State the preparation type.
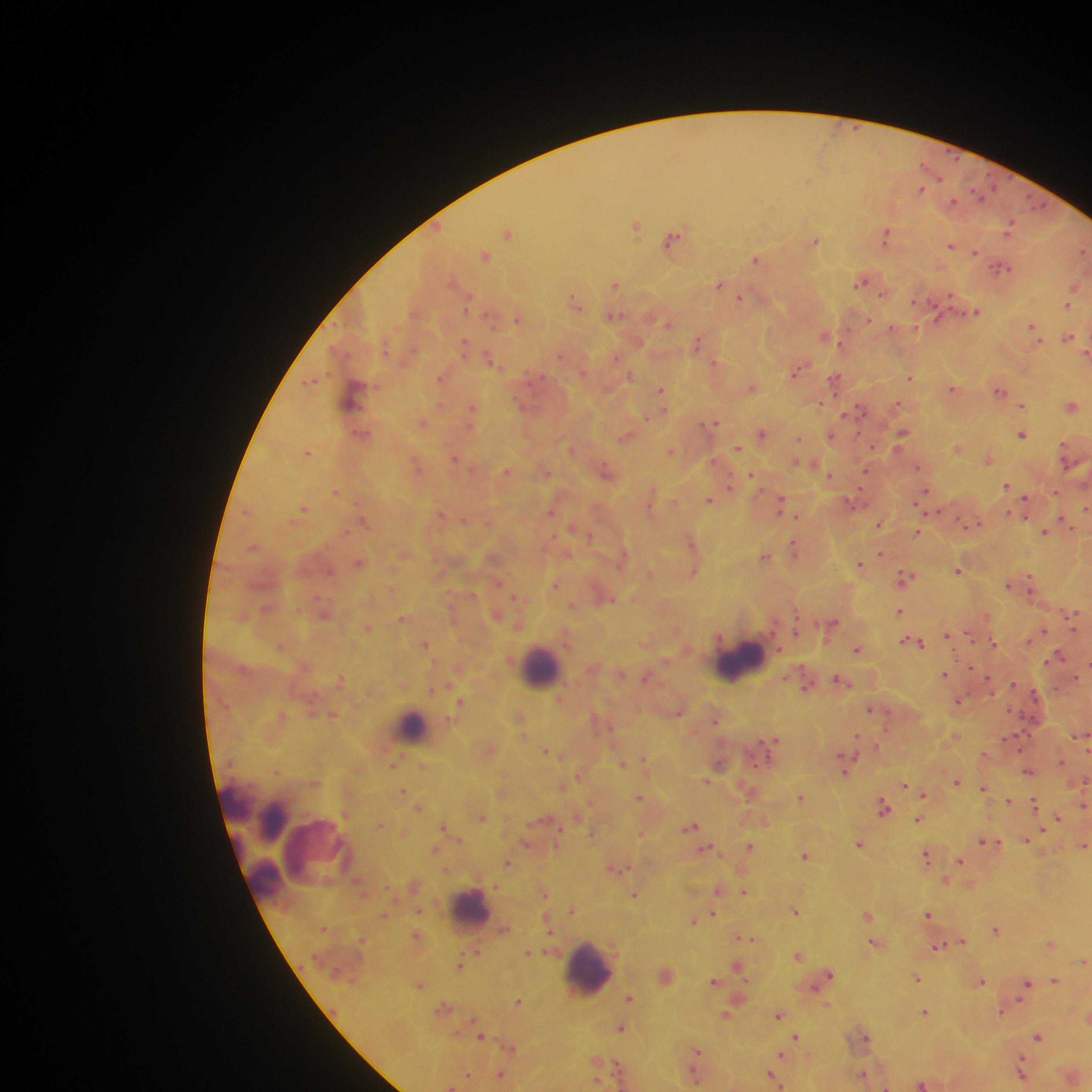

This is a thick smear.

{
  "field_of_view": "single",
  "leukocyte_locations": "approximate centers as x y in pixels: 733 661; 542 665; 415 724; 468 913; 584 968",
  "country": "Ghana",
  "plasmodium_parasite_locations": "approximate centers as x y in pixels: 957 157; 929 168; 922 189; 976 190; 1041 206; 1014 221; 637 225; 508 235; 1009 235; 886 236; 671 239; 815 239; 951 247; 976 252; 1083 252; 485 255; 755 259; 1009 267; 860 282; 616 283; 719 286; 1075 286; 883 294; 741 296; 574 297; 1068 305; 976 311; 486 314; 869 319; 668 323; 1033 325; 826 336; 1069 336; 464 340; 699 340; 840 344; 1086 351; 487 355; 800 369; 631 374; 441 377; 910 377; 835 379; 308 381; 660 389; 1001 390; 898 403; 441 404; 519 404; 821 404; 1022 405; 473 406; 1073 406; 846 414; 646 417; 717 421; 425 422; 708 424; 858 432; 903 432; 761 433; 832 434; 1022 434; 800 439; 872 444; 739 447; 308 454; 455 459; 989 460; 716 462; 918 467; 508 471; 865 471; 549 473; 729 473; 753 473; 830 475; 1007 486; 730 487; 861 490; 925 490; 336 493; 1055 493; 1026 496; 709 500; 781 500; 357 503; 1085 508; 304 509; 550 512; 781 512; 1008 512; 249 514; 441 514; 795 515; 1061 518; 363 521; 463 522; 573 527; 1075 529; 1045 532; 554 536; 589 536; 793 543; 692 544; 254 547; 567 554; 881 554; 767 556; 861 563; 959 569; 329 572; 906 575; 499 581; 1031 582; 555 584; 1010 585; 516 595; 317 597; 265 608; 900 610; 322 616; 1074 630; 795 631; 1046 631; 947 635; 970 636; 912 640; 1028 641; 921 643; 993 643; 426 645; 280 647; 778 650; 856 650; 1059 653; 971 667; 945 674; 836 677; 988 677; 342 678; 1013 685; 431 689; 1034 693; 461 700; 959 702; 870 710; 1013 711; 678 713; 333 714; 279 716; 716 719; 884 726; 857 734; 769 742; 877 745; 763 746; 856 755; 844 756; 644 757; 623 763; 277 771; 1029 771; 578 773; 317 782; 958 782; 904 785; 984 787; 403 790; 924 795; 640 796; 1009 800; 1034 803; 884 804; 1084 805; 419 807; 345 813; 1057 816; 482 817; 919 820; 380 823; 443 826; 692 826; 561 827; 1042 829; 590 835; 459 839; 982 841; 999 841; 1026 841; 525 844; 749 845; 1084 847; 926 854; 805 856; 960 862; 509 863; 621 869; 497 886; 719 890; 745 891; 545 894; 634 895; 571 909; 416 910; 797 910; 712 911; 929 914; 867 915; 384 916; 694 921; 996 931; 550 933; 363 937; 740 937; 754 937; 746 938; 963 941; 939 947; 528 952; 798 956; 1082 961; 737 964; 458 966; 831 975; 747 978; 918 978; 1056 978; 983 980; 715 981; 1028 983; 420 986; 630 998; 1019 999; 519 1001; 826 1004; 924 1013; 1000 1013; 779 1016; 470 1019; 621 1028; 797 1035; 481 1036; 1039 1036; 866 1038; 511 1049; 699 1049; 782 1055; 1022 1056; 597 1059; 617 1063; 694 1069; 502 1073; 863 1073; 1023 1073; 468 1074; 772 1074; 780 1084; 922 1084; 887 1086",
  "image_size": "1092×1092 pixels",
  "capture": "mobile-phone photograph through a microscope"
}